Report the malaria status of this cell.
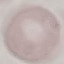

It is uninfected.

Summary:
  - Stain: Giemsa
  - Image type: automatically extracted cell patch, resized to 64 × 64 pixels
  - Preparation: thin blood film
  - Capture: smartphone camera at the microscope eyepiece